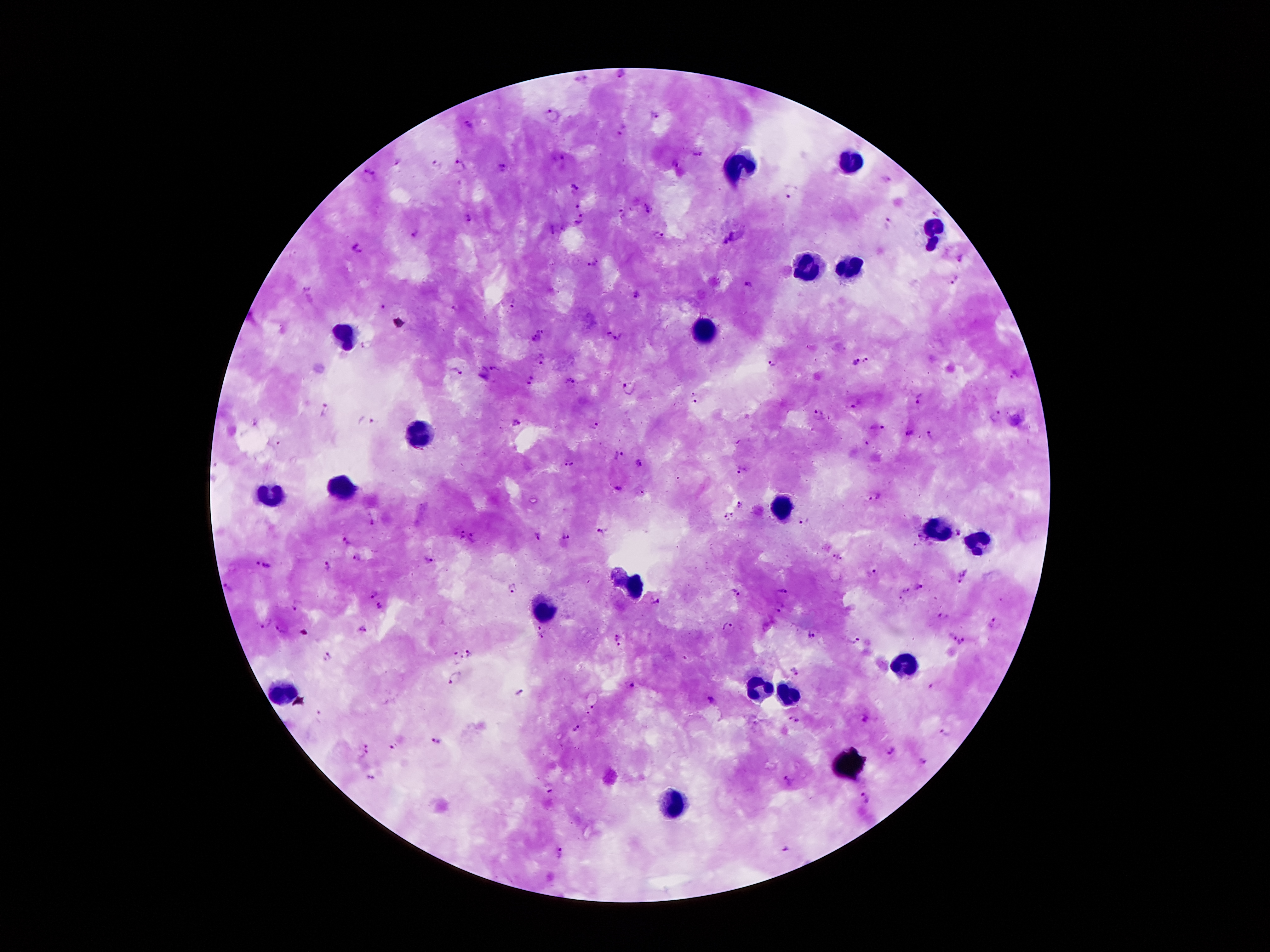
Approximate centers as [x, y] in pixels. Leukocyte locations: [851, 159], [737, 165], [931, 235], [805, 265], [849, 265], [705, 329], [343, 333], [425, 433], [341, 487], [267, 495], [783, 507], [937, 527], [977, 541], [627, 579], [545, 607], [907, 665], [757, 687], [281, 693], [789, 697], [679, 801]. Plasmodium parasite locations: [621, 75], [552, 113], [657, 115], [470, 124], [696, 152], [396, 162], [676, 163], [438, 164], [459, 167], [503, 168], [368, 175], [577, 185], [791, 191], [577, 207], [649, 209], [938, 213], [468, 216], [579, 220], [888, 222], [415, 235], [659, 236], [356, 248], [959, 258], [591, 263], [955, 280], [747, 286], [307, 289], [637, 296], [513, 304], [383, 307], [453, 308], [543, 331], [606, 331], [616, 338], [534, 339], [542, 360], [854, 361], [866, 361], [771, 363], [495, 368], [453, 372], [1013, 373], [531, 378], [570, 380], [628, 389], [696, 399], [919, 399], [856, 404], [325, 411], [819, 413], [997, 418], [366, 422], [516, 422], [595, 426], [875, 429], [908, 434], [931, 436], [278, 444], [618, 456], [569, 461], [637, 462], [742, 473], [877, 496], [740, 504], [727, 516], [803, 520], [371, 522], [603, 533], [462, 536], [537, 537], [346, 538], [565, 538], [474, 539], [917, 544], [358, 556], [835, 557], [430, 564], [328, 565], [264, 566], [873, 573], [964, 577], [511, 587], [230, 588], [920, 588], [785, 589], [904, 590], [372, 594], [735, 594], [900, 600], [656, 604], [298, 606], [780, 606], [379, 607], [943, 619], [263, 622], [994, 622], [728, 626], [280, 627], [362, 627], [544, 633], [814, 633], [616, 635], [951, 637], [854, 641], [964, 642], [620, 648], [470, 652], [330, 655], [458, 657], [793, 669], [455, 680], [630, 686], [936, 688], [521, 694], [711, 701], [591, 711], [790, 722], [577, 732], [947, 733], [436, 741], [391, 744], [367, 748], [892, 750], [922, 760], [368, 775], [790, 782], [550, 788], [865, 798], [783, 850], [559, 851]. Giemsa-stained preparation. Patient malaria status: positive for Plasmodium falciparum. Smartphone photograph taken through the microscope eyepiece. Thick blood smear. 100x magnification. Single field of view. Image is 1270×952 pixels.